Assess this cell for malaria.
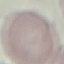
It is uninfected.

stain = Giemsa
capture = smartphone through the microscope eyepiece
preparation = thin blood film
image type = cell patch, automatically extracted from a larger field of view and resized to 64 × 64 pixels